Locate every blood parasite and identify its species.
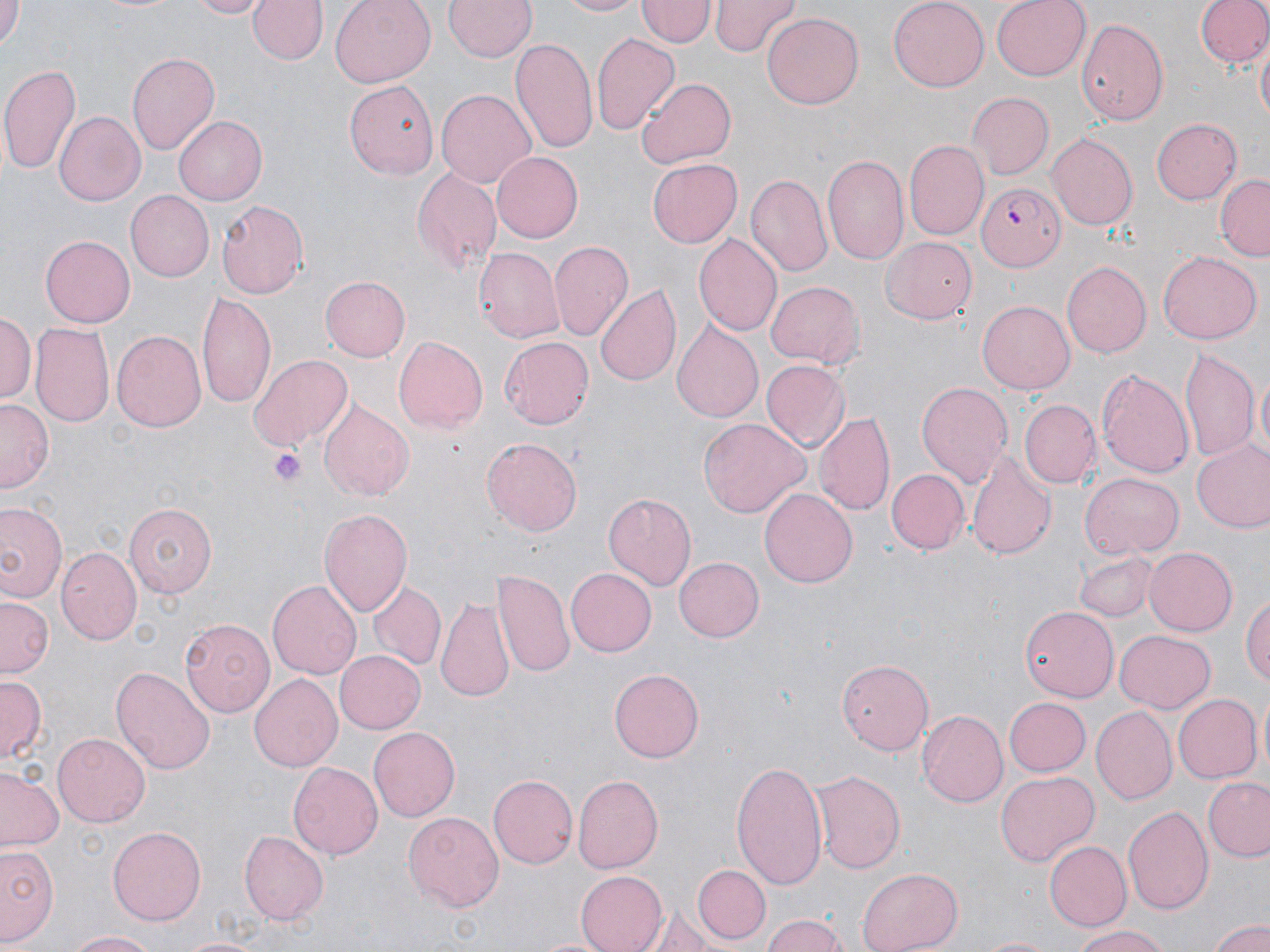

Approximate bounding boxes as [x1, y1, x2, y2] in pixels.
Plasmodium falciparum-infected red blood cells: [979, 180, 1066, 272].
No Plasmodium ovale, Plasmodium malariae, Plasmodium vivax, Babesia divergens, or Trypanosoma brucei observed.

Platelet locations: [268, 446, 306, 489]. Uninfected red blood cell locations: [0, 0, 22, 50], [187, 0, 272, 19], [247, 0, 327, 67], [327, 0, 436, 88], [444, 0, 536, 62], [552, 0, 645, 17], [639, 0, 712, 49], [710, 0, 798, 56], [887, 0, 989, 90], [991, 0, 1089, 79], [1190, 0, 1270, 73], [92, 1, 185, 15], [762, 13, 865, 109], [1076, 17, 1169, 125], [591, 32, 679, 136], [511, 39, 596, 157], [1256, 41, 1269, 128], [128, 52, 220, 155], [1, 64, 82, 178], [637, 77, 737, 171], [344, 78, 439, 179], [437, 89, 535, 190], [967, 92, 1052, 179], [55, 110, 145, 206], [175, 116, 268, 208], [1152, 118, 1243, 203], [1046, 133, 1136, 230], [904, 140, 988, 240], [490, 150, 583, 243], [821, 153, 910, 266], [645, 159, 741, 248], [413, 167, 501, 275], [744, 175, 831, 276], [1216, 175, 1270, 261], [123, 191, 213, 281], [216, 200, 308, 300], [693, 233, 782, 337], [39, 235, 134, 327], [882, 236, 976, 323], [549, 239, 633, 342], [474, 249, 563, 340], [1158, 252, 1262, 345], [1062, 260, 1151, 359], [321, 277, 410, 361], [766, 281, 865, 370], [597, 284, 680, 387], [198, 291, 275, 410], [976, 300, 1073, 395], [1, 310, 35, 404], [672, 322, 762, 423], [30, 323, 114, 431], [112, 328, 206, 429], [391, 335, 487, 434], [499, 335, 594, 428], [1181, 350, 1258, 463], [248, 353, 353, 451], [761, 361, 849, 450], [1098, 365, 1196, 483], [1252, 369, 1269, 469], [916, 381, 1013, 488], [1, 399, 54, 492], [319, 400, 414, 499], [1019, 400, 1099, 487], [817, 410, 895, 515], [700, 418, 808, 518], [483, 437, 582, 537], [1192, 441, 1270, 534], [966, 451, 1054, 561], [887, 468, 969, 554], [1081, 472, 1182, 559], [760, 488, 858, 589], [603, 492, 696, 590], [0, 501, 65, 603], [124, 503, 215, 598], [321, 508, 413, 617], [1145, 545, 1239, 635], [57, 547, 141, 647], [1074, 551, 1160, 622], [674, 557, 764, 642], [564, 567, 657, 656], [492, 572, 574, 678], [366, 579, 445, 670], [267, 581, 361, 681], [1242, 590, 1270, 692], [1, 595, 54, 680], [437, 595, 512, 701], [1020, 607, 1119, 702], [180, 617, 276, 714], [1116, 629, 1216, 712], [332, 648, 425, 735], [837, 657, 933, 756], [110, 665, 215, 776], [609, 667, 706, 763], [248, 673, 341, 773], [0, 678, 44, 762], [1171, 693, 1261, 783], [1002, 697, 1090, 776], [1091, 707, 1177, 807], [916, 710, 1007, 807], [369, 726, 460, 821], [53, 732, 150, 824], [730, 759, 827, 890], [289, 761, 384, 861], [808, 767, 905, 872], [0, 769, 64, 854], [994, 770, 1099, 868], [487, 774, 577, 871], [573, 775, 663, 873], [1203, 777, 1270, 862], [1121, 802, 1214, 914], [403, 809, 504, 911], [108, 826, 207, 925], [239, 830, 329, 925], [1042, 840, 1130, 932], [1, 841, 60, 947], [693, 864, 770, 943], [857, 865, 963, 952], [573, 870, 667, 952], [647, 910, 718, 951], [760, 912, 848, 952], [1210, 921, 1270, 952], [1069, 925, 1173, 951], [65, 929, 156, 951], [976, 934, 1057, 952]. Slide-level diagnosis: Plasmodium falciparum. Image is 1270×952 pixels. Light microscopy. Thin blood smear. 1000x magnification. May-Grünwald-Giemsa stain. One field of a larger specimen.